Report the malaria status of this cell.
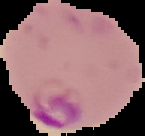
Parasitized.

image size = 145×136 pixels
image type = cell region segmented out of the field of view; surrounding area masked to black
preparation = thin blood smear